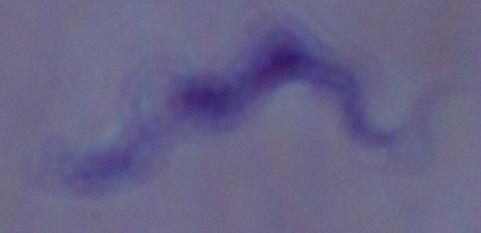
magnification = 1000x
modality = micrograph
identification = trypanosome